Assess this cell for malaria.
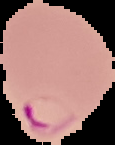

It is parasitized.

Summary:
  - Image type: segmented cell region with the area outside set to black
  - Preparation: thin blood smear
  - Image size: 115×145 pixels